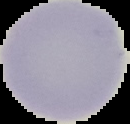
Summary:
  - Preparation: thin blood film
  - Image type: segmented cell region with the area outside set to black
  - Image size: 130×124 pixels
  - Malaria status: uninfected